Identify the parasite.
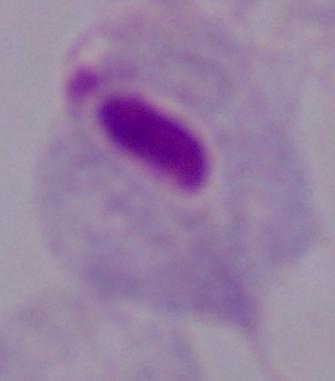
This is a trichomonad.

Captured at 1000x magnification. Micrograph.